Classify this cell by malaria status.
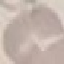

It is uninfected.

preparation = thin smear
stain = Giemsa
image type = cell patch, automatically extracted from a larger field of view and resized to 64 × 64 pixels
capture = smartphone camera at the microscope eyepiece